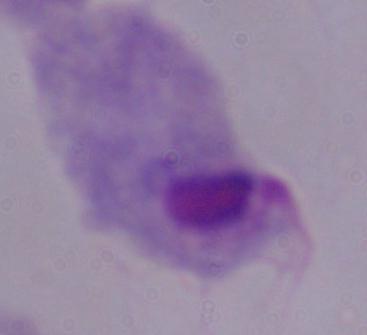 Captured at 1000x magnification. Micrograph. A trichomonad is seen.